Point out each leukocyte.
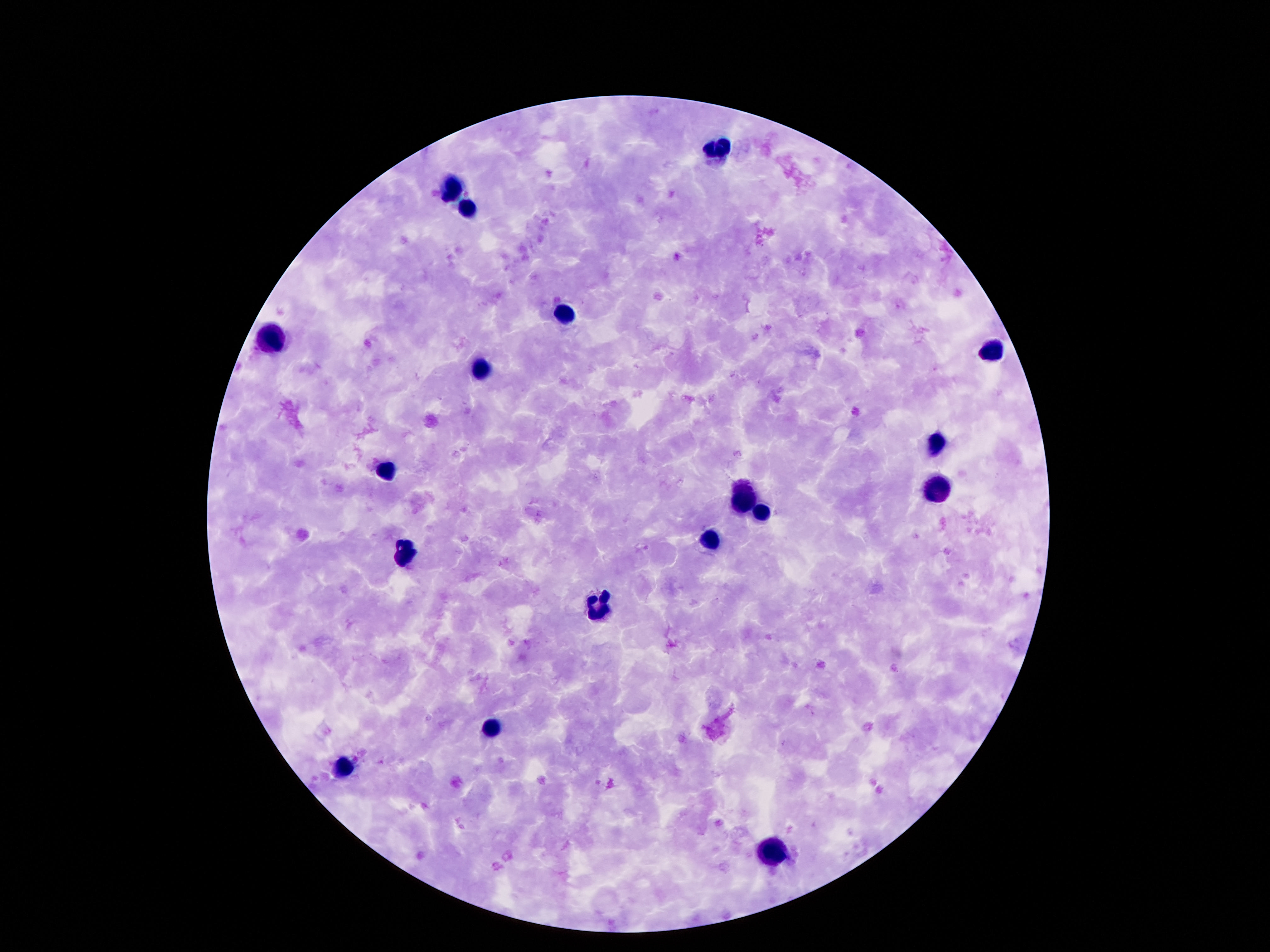
Approximate object centers, in pixels from the top-left corner.
Leukocytes: (x=715, y=149), (x=453, y=190), (x=468, y=211), (x=560, y=315), (x=269, y=339), (x=993, y=352), (x=483, y=369), (x=937, y=444), (x=388, y=470), (x=937, y=487), (x=746, y=498), (x=765, y=513), (x=709, y=541), (x=403, y=554), (x=601, y=606), (x=489, y=729), (x=343, y=765), (x=767, y=853).

field of view = single
image size = 1270×952 pixels
magnification = 100x
capture = smartphone camera through the microscope eyepiece
preparation = thick peripheral-blood smear
patient malaria status = negative
stain = Giemsa